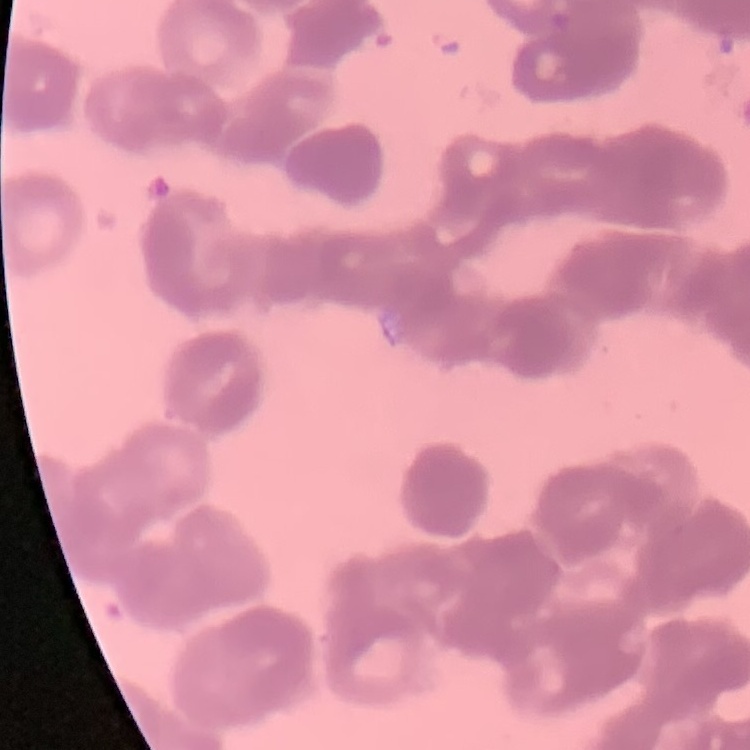

The erythrocytes exhibit rouleaux formation. Square crop of a larger photomicrograph. Thin blood smear. Field's or Giemsa stain.